Give the position of every malaria parasite and every leukocyte.
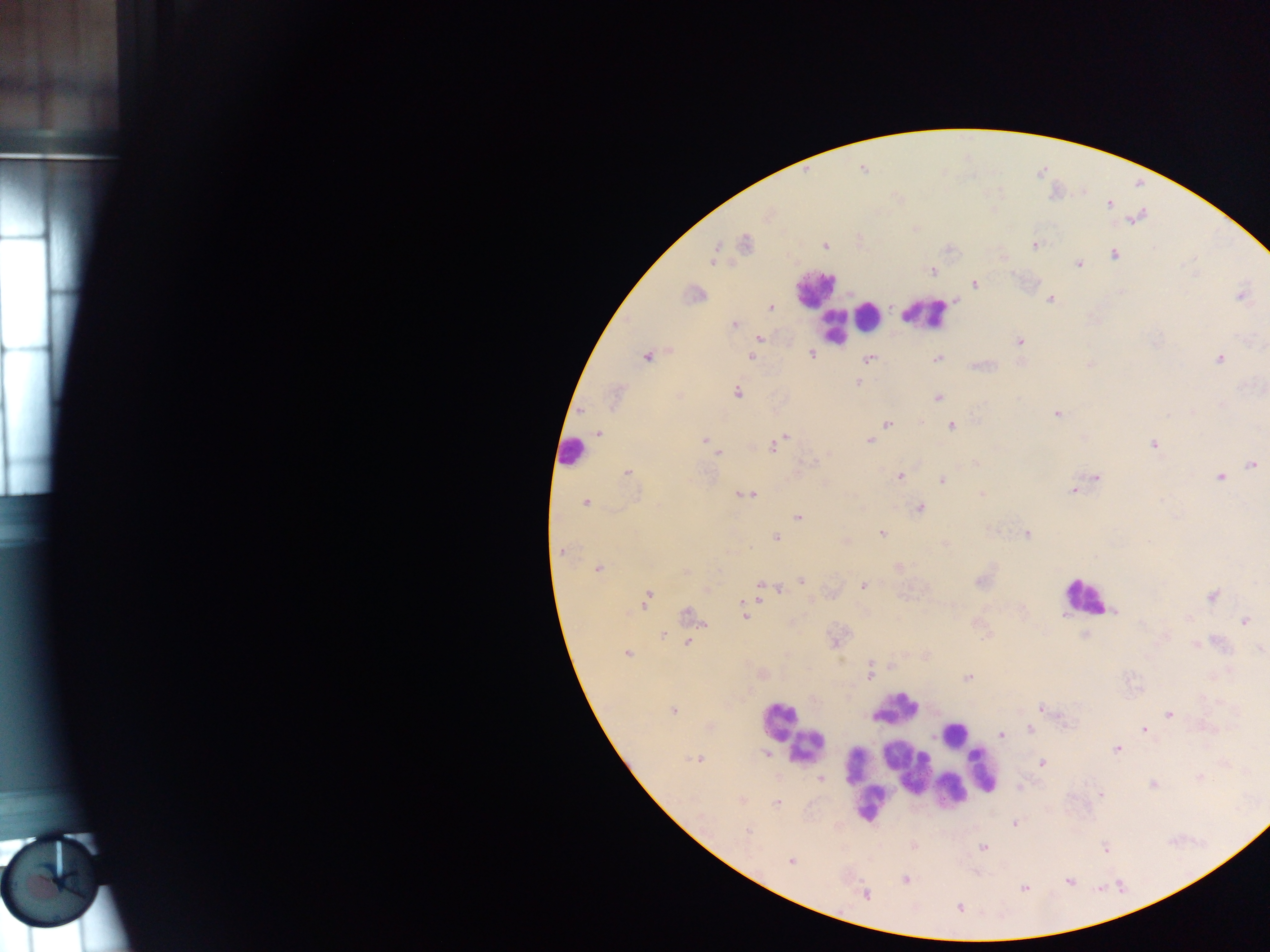
Approximate centers as {x, y} in pixels.
Malaria parasites: {863, 169}, {1109, 204}, {1136, 218}, {745, 243}, {1034, 245}, {825, 246}, {1114, 255}, {714, 257}, {1079, 263}, {932, 271}, {975, 284}, {694, 294}, {1242, 296}, {1050, 299}, {770, 307}, {734, 325}, {760, 338}, {1019, 341}, {812, 354}, {646, 357}, {751, 357}, {938, 357}, {870, 358}, {1219, 358}, {1090, 365}, {858, 383}, {737, 392}, {615, 397}, {938, 398}, {1057, 413}, {887, 424}, {951, 426}, {599, 433}, {783, 439}, {705, 441}, {869, 441}, {1155, 444}, {709, 446}, {775, 446}, {717, 452}, {813, 462}, {1252, 465}, {627, 473}, {900, 476}, {1220, 477}, {1096, 478}, {942, 479}, {1073, 490}, {746, 494}, {981, 494}, {586, 503}, {920, 509}, {798, 516}, {881, 533}, {1027, 534}, {776, 537}, {562, 550}, {598, 570}, {685, 571}, {802, 580}, {981, 581}, {863, 586}, {760, 587}, {767, 588}, {779, 589}, {1212, 596}, {648, 597}, {743, 606}, {1114, 611}, {688, 613}, {744, 614}, {1245, 621}, {663, 635}, {1084, 635}, {687, 642}, {1196, 645}, {1261, 649}, {627, 654}, {870, 674}, {968, 677}, {1043, 709}, {674, 711}, {1169, 714}, {1063, 718}, {1030, 729}, {1145, 730}, {1001, 735}, {1117, 749}, {767, 753}, {698, 759}, {1042, 763}, {1200, 778}, {821, 779}, {1153, 785}, {1100, 794}, {740, 801}, {776, 803}, {1015, 823}, {747, 831}, {982, 848}, {1106, 849}, {791, 861}, {905, 879}, {1068, 881}, {1024, 888}, {866, 894}, {959, 908}.
Leukocytes: {815, 288}, {869, 315}, {925, 315}, {833, 327}, {570, 451}, {1083, 596}, {897, 708}, {778, 720}, {954, 733}, {807, 746}, {907, 767}, {983, 769}, {861, 781}, {952, 790}, {867, 802}.

country = Ghana
field of view = single
preparation = thick blood smear
image size = 1270×952 pixels
capture = mobile-phone photograph through a microscope